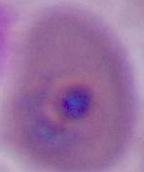

Summary:
  - Modality: photomicrograph
  - Magnification: 400x or 1000x
  - Identification: Plasmodium